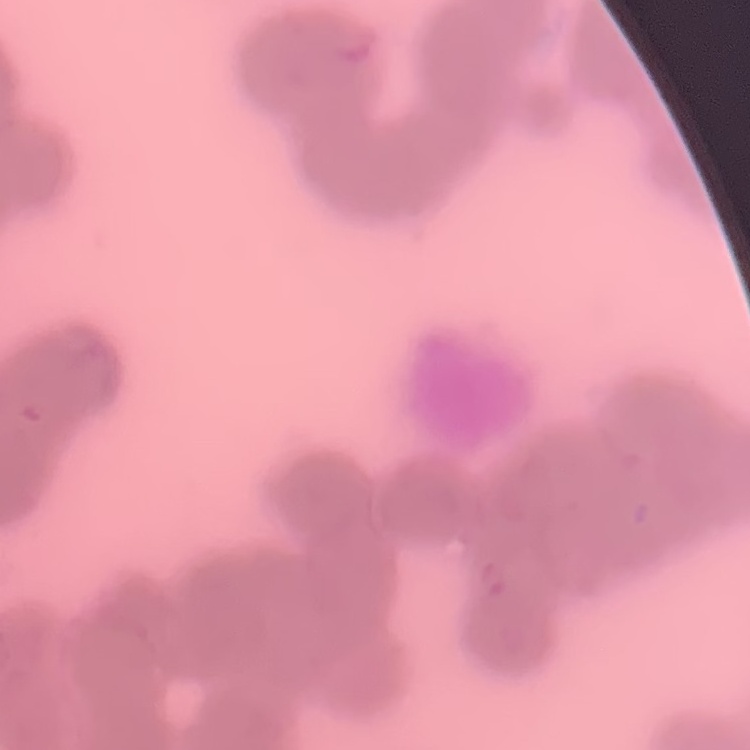

Summary:
  - Red blood cell morphology: rouleaux formation
  - Preparation: thin peripheral smear
  - Image type: square crop of a larger photomicrograph
  - Stain: Field's or Giemsa